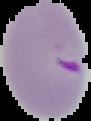
Result: malaria parasites detected. Image is 91×121 pixels. From a thin blood smear. The area outside the segmented cell region is set to black.